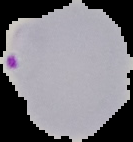

Summary:
  - Result: malaria parasites identified
  - Image size: 133×142 pixels
  - Image type: segmented cell region with the area outside set to black
  - Preparation: thin blood smear